Classify this cell by malaria status.
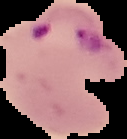

It is parasitized.

preparation = thin blood smear
image size = 127×139 pixels
image type = cell region segmented out of the field of view; surrounding area masked to black